Report the malaria status of this cell.
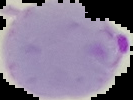
Parasitized.

From a thin blood smear. Image is 133×100 pixels. Segmented cell region on a black background.